Outline each blood parasite and name the species.
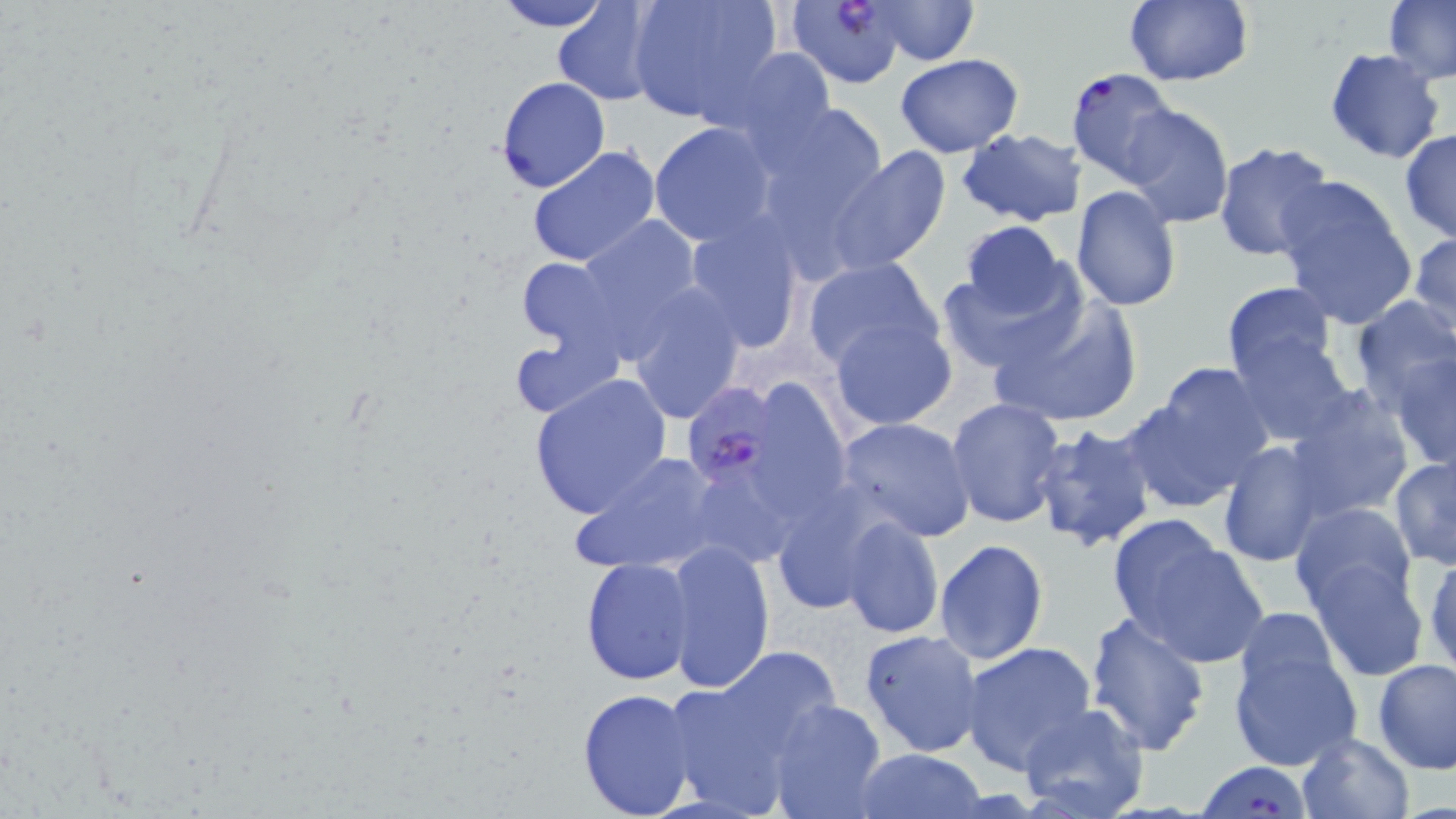

Approximate bounding boxes as (x1, y1, x2, y2) in pixels.
Plasmodium falciparum-infected red blood cells: (786, 0, 912, 89), (1064, 66, 1175, 186), (684, 382, 776, 488), (1200, 762, 1311, 816).
No Plasmodium ovale, Plasmodium malariae, Plasmodium vivax, Babesia divergens, or Trypanosoma brucei observed.

Summary:
  - Uninfected red blood cell locations: (490, 0, 616, 31), (624, 0, 784, 125), (866, 0, 978, 64), (1124, 0, 1253, 87), (1383, 0, 1456, 84), (552, 1, 666, 105), (720, 46, 837, 147), (1324, 48, 1445, 164), (895, 54, 1025, 157), (495, 76, 610, 193), (752, 100, 889, 235), (1118, 105, 1234, 229), (649, 123, 777, 245), (957, 128, 1087, 227), (1399, 129, 1456, 242), (1212, 140, 1338, 265), (525, 144, 661, 268), (829, 147, 951, 275), (1274, 174, 1419, 330), (1070, 187, 1181, 312), (570, 213, 710, 357), (682, 215, 807, 354), (960, 219, 1070, 321), (1408, 230, 1456, 342), (936, 253, 1087, 375), (515, 257, 620, 354), (802, 257, 945, 373), (1222, 282, 1340, 388), (623, 284, 746, 425), (986, 292, 1143, 429), (1349, 295, 1456, 412), (829, 315, 956, 429), (1228, 324, 1355, 446), (510, 332, 620, 420), (1390, 351, 1456, 472), (1135, 364, 1279, 508), (527, 373, 672, 520), (1285, 386, 1415, 523), (945, 397, 1066, 528), (835, 417, 976, 541), (1032, 422, 1158, 553), (1217, 440, 1330, 567), (571, 450, 726, 576), (1389, 455, 1456, 568), (770, 491, 885, 618), (1290, 502, 1420, 619), (1107, 514, 1263, 667), (838, 516, 944, 639), (662, 538, 776, 694), (934, 538, 1048, 665), (1424, 551, 1456, 681), (580, 556, 698, 686), (1310, 558, 1427, 681), (1083, 610, 1212, 757), (1228, 626, 1362, 773), (858, 627, 985, 758), (961, 641, 1099, 775), (669, 651, 840, 805), (1373, 657, 1456, 773), (577, 687, 700, 819), (765, 699, 887, 819), (1016, 703, 1151, 819), (1297, 732, 1416, 819), (855, 747, 986, 818)
  - Slide-level diagnosis: Plasmodium falciparum
  - Preparation: thin blood film
  - Stain: May-Grünwald-Giemsa
  - Field of view: single
  - Magnification: 1000x
  - Image size: 1456×819 pixels
  - Modality: optical microscopy